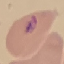 Result: malaria parasites detected. Thin smear of blood. Automatically extracted cell patch, resized to 64 × 64 pixels. Giemsa-stained preparation. Acquired by smartphone through the microscope eyepiece.